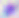
Summary:
  - Magnification: 400x
  - Modality: photomicrograph
  - Identification: Toxoplasma gondii